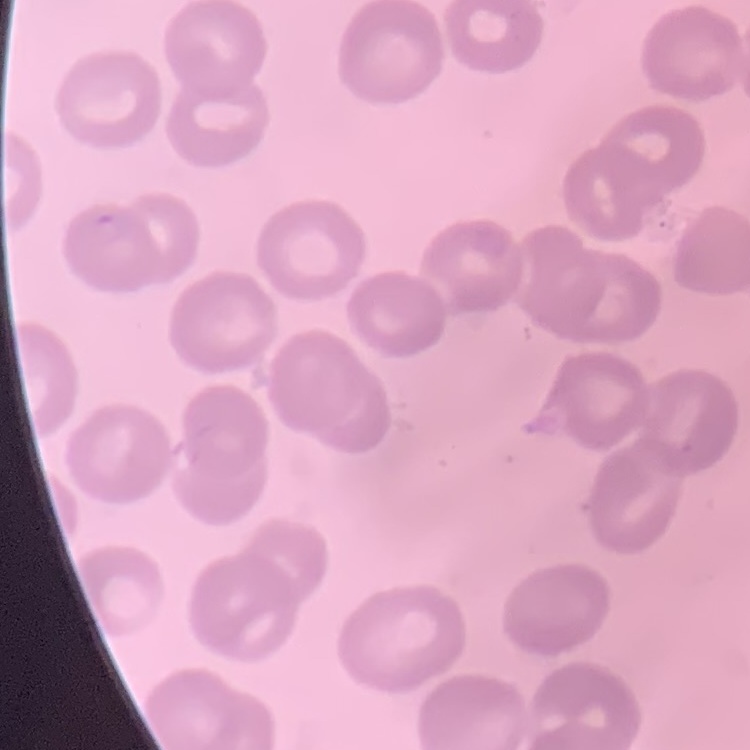 The red blood cells show no rouleaux formation. Stained with either Field's or Giemsa. Square crop of a larger photomicrograph. Thin blood smear.